Identify the parasite.
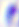

This is Toxoplasma gondii.

magnification: 400x
modality: photomicrograph